Classify this cell by malaria status.
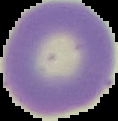
Uninfected.

{
  "preparation": "thin blood smear",
  "image_size": "118×121 pixels",
  "image_type": "cell region segmented out of the field of view; surrounding area masked to black"
}